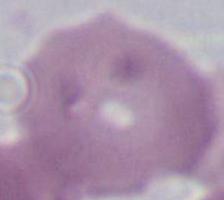

Summary:
  - Identification: red blood cell
  - Magnification: 1000x
  - Modality: micrograph